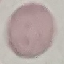 Result: negative for malaria parasites. Giemsa-stained preparation. Acquired by smartphone through the microscope eyepiece. Thin smear of blood. Automatically extracted cell patch, resized to 64 × 64 pixels.